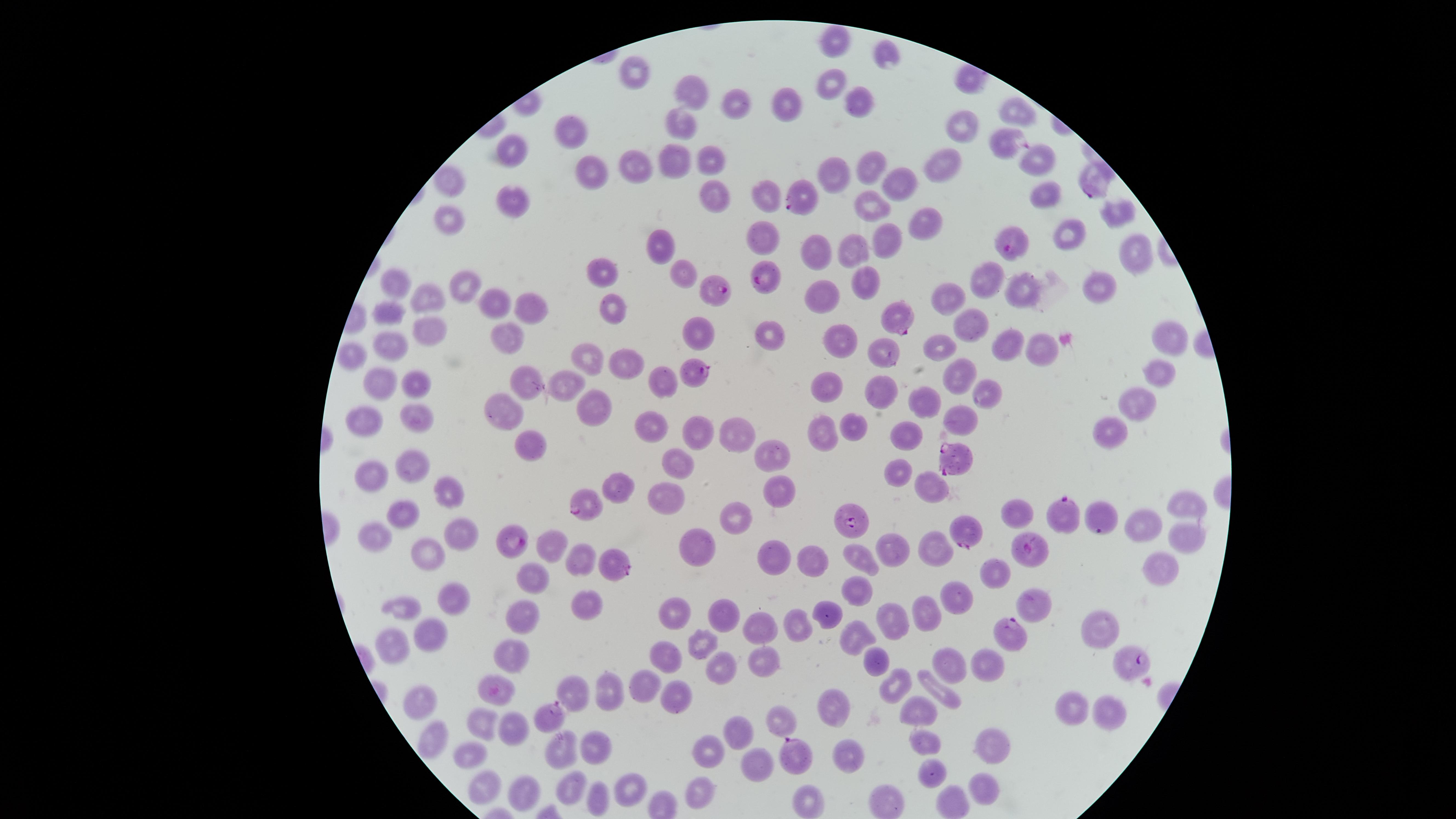

Approximate marker points as [x, y] in pixels.
Summary:
  - Uninfected red blood cells: [833, 42], [886, 57], [635, 70], [832, 79], [696, 87], [737, 101], [785, 106], [863, 106], [1016, 110], [683, 122], [958, 128], [573, 131], [513, 145], [710, 157], [676, 159], [1037, 159], [636, 162], [942, 165], [868, 166], [589, 167], [833, 171], [450, 182], [894, 183], [716, 192], [766, 194], [1048, 194], [508, 200], [868, 209], [1113, 212], [455, 218], [924, 224], [767, 231], [1067, 232], [885, 238], [818, 243], [661, 244], [1135, 249], [853, 251], [606, 272], [984, 276], [687, 278], [863, 278], [1027, 283], [1101, 283], [396, 287], [464, 287], [826, 292], [430, 296], [496, 299], [946, 300], [528, 305], [611, 305], [387, 314], [963, 325], [427, 330], [767, 331], [699, 332], [510, 334], [1168, 339], [840, 340], [1001, 343], [937, 345], [391, 346], [1037, 349], [352, 353], [590, 359], [628, 367], [1159, 373], [957, 375], [385, 380], [567, 381], [661, 383], [412, 385], [521, 385], [825, 385], [875, 391], [922, 394], [982, 394], [1135, 399], [603, 403], [509, 414], [416, 416], [360, 423], [647, 423], [955, 425], [824, 426], [846, 427], [694, 428], [1110, 430], [734, 433], [906, 436], [526, 440], [773, 456], [674, 463], [413, 464], [368, 472], [903, 472], [625, 483], [779, 486], [929, 490], [451, 491], [1184, 498], [666, 504], [1014, 510], [401, 511], [741, 511], [1142, 523], [460, 526], [1185, 530], [371, 534], [699, 538], [548, 543], [936, 545], [894, 546], [863, 551], [432, 553], [579, 555], [774, 556], [815, 557], [999, 568], [1157, 568], [537, 575], [855, 585], [450, 590], [952, 600], [1037, 601], [582, 602], [409, 603], [523, 606], [833, 612], [923, 612], [682, 614], [727, 614], [897, 620], [761, 624], [800, 624], [1101, 626], [426, 629], [854, 637], [397, 638], [699, 638], [512, 647], [672, 653], [879, 657], [947, 660], [762, 661], [983, 664], [722, 668], [650, 677], [492, 681], [892, 685], [576, 688], [944, 690], [611, 691], [673, 694], [424, 699], [922, 700], [1073, 705], [838, 707], [1102, 713], [779, 721], [478, 725], [512, 730], [736, 730], [919, 738], [425, 740], [988, 740], [560, 745], [593, 745], [710, 750], [849, 750], [471, 756], [753, 762], [933, 768], [569, 778], [627, 784], [982, 786], [704, 787], [489, 789], [518, 793], [942, 797], [590, 798], [809, 799], [888, 804]
  - Parasitized red blood cells: [1000, 141], [1091, 189], [803, 197], [1009, 239], [768, 276], [716, 290], [900, 317], [887, 353], [698, 368], [954, 456], [587, 501], [1067, 516], [857, 519], [966, 530], [514, 538], [1027, 552], [618, 565], [1009, 633], [1134, 665], [546, 715], [799, 754]
  - Presence: malaria parasites detected
  - Capture: smartphone photograph through the microscope eyepiece
  - Species: Plasmodium falciparum
  - Preparation: thin blood smear
  - Field of view: single
  - Image size: 1456×819 pixels
  - Stain: Giemsa
  - Visible region: circular